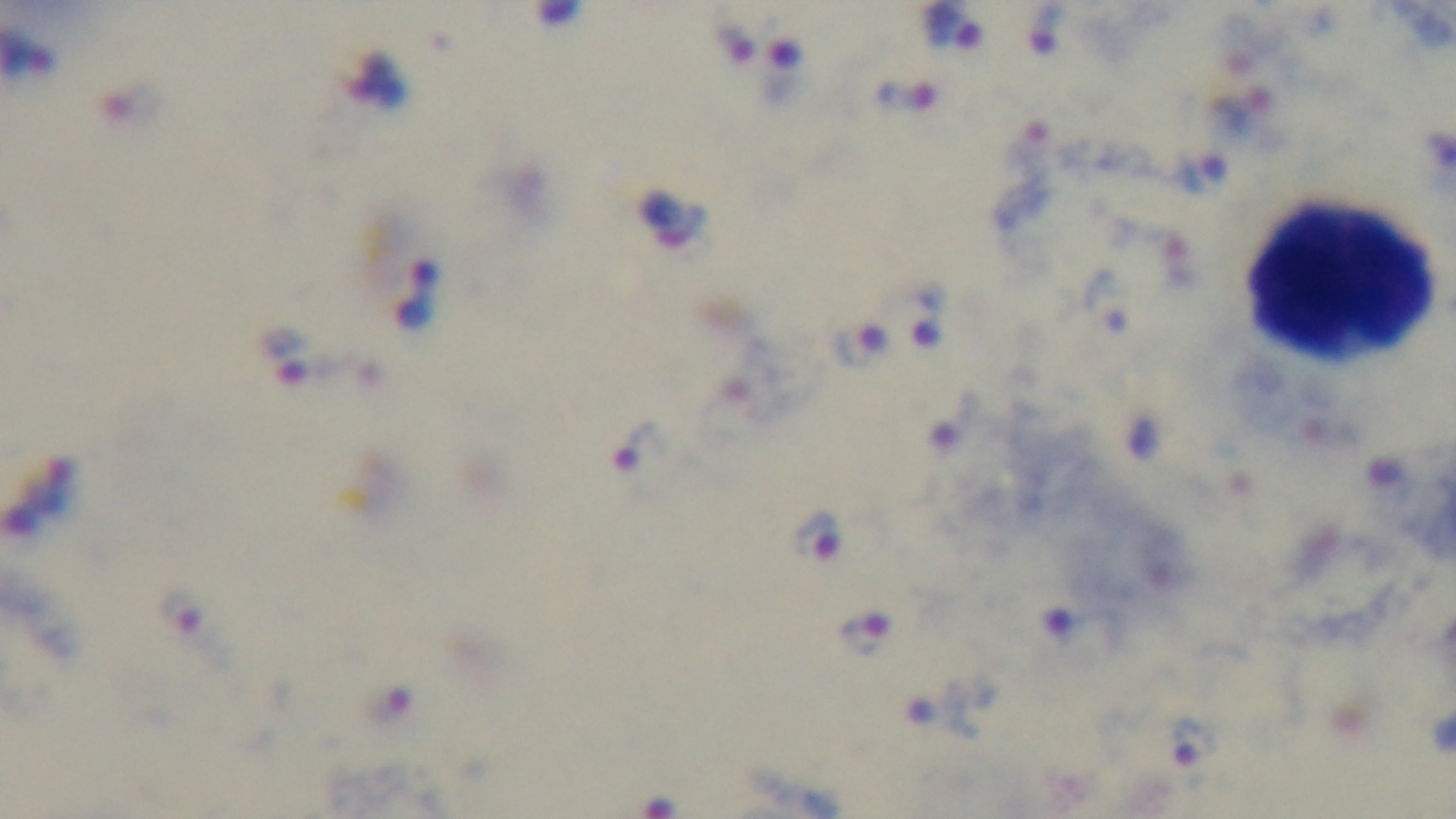

Summary:
  - Capture: mounted 4K digital camera
  - Objective: 100x oil immersion
  - Preparation: thick smear
  - Stain: Giemsa
  - Malaria status: infected
  - Field of view: one from the slide
  - Modality: light microscopy